Report the malaria status of this cell.
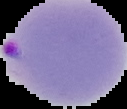

Parasitized.

From a thin blood film. Image is 127×109 pixels. Segmented cell region on a black background.